Report the malaria status of this cell.
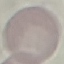

It is uninfected.

image type = automatically extracted cell patch, resized to 64 × 64 pixels
stain = Giemsa
preparation = thin blood smear
capture = smartphone through the microscope eyepiece